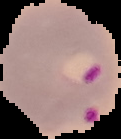
image size = 121×139 pixels
image type = segmented cell region on a black background
preparation = thin blood film
result = Plasmodium parasites identified